Classify this cell by malaria status.
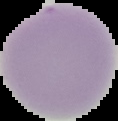
It is uninfected.

Cell region segmented out of the field of view; the surrounding area is masked to black. Image is 118×121 pixels. From a thin blood film.